Assess this cell for malaria.
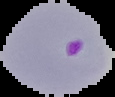

Parasitized.

Summary:
  - Image size: 115×97 pixels
  - Preparation: thin blood film
  - Image type: segmented cell region with the area outside set to black